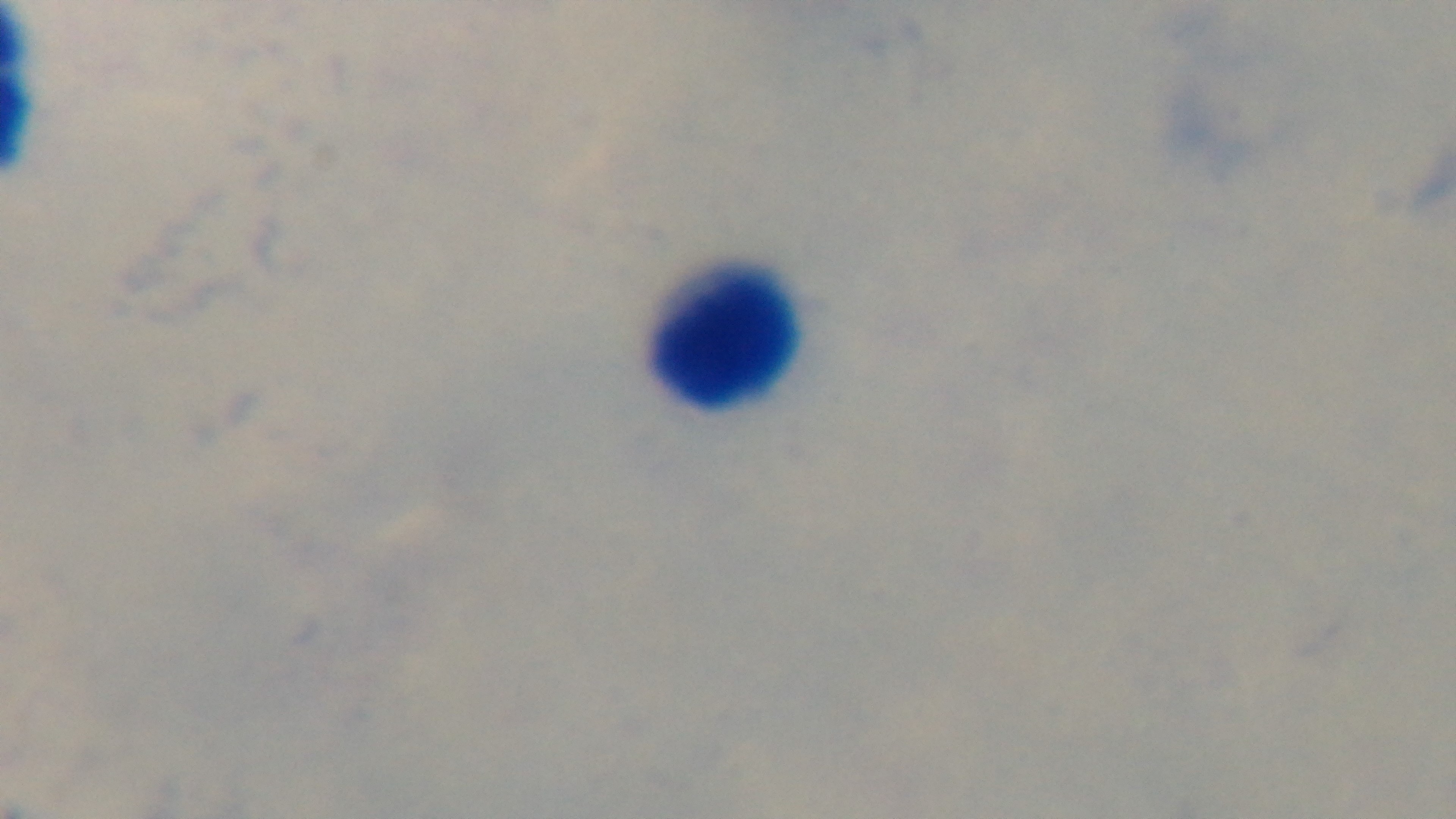

stain = Giemsa
capture = mounted 4K digital camera
objective = 100x oil immersion
field of view = single
preparation = thick blood film
modality = light microscopy
malaria status = uninfected